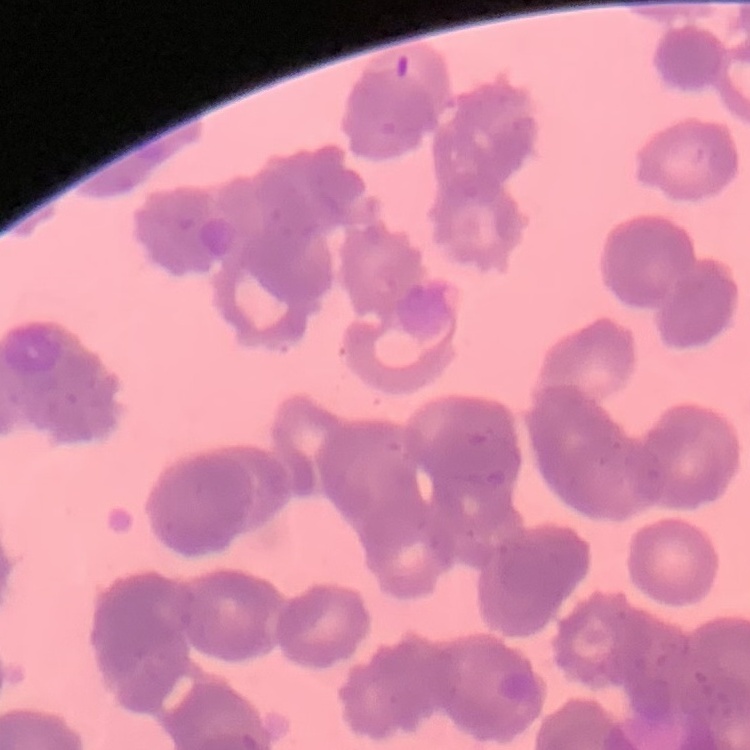

The erythrocytes exhibit rouleaux formation. Field's or Giemsa stain. One tile cut from a larger photomicrograph. Thin blood smear.